Name the parasite shown.
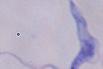
This is a trypanosome.

1000x magnification. Photomicrograph.